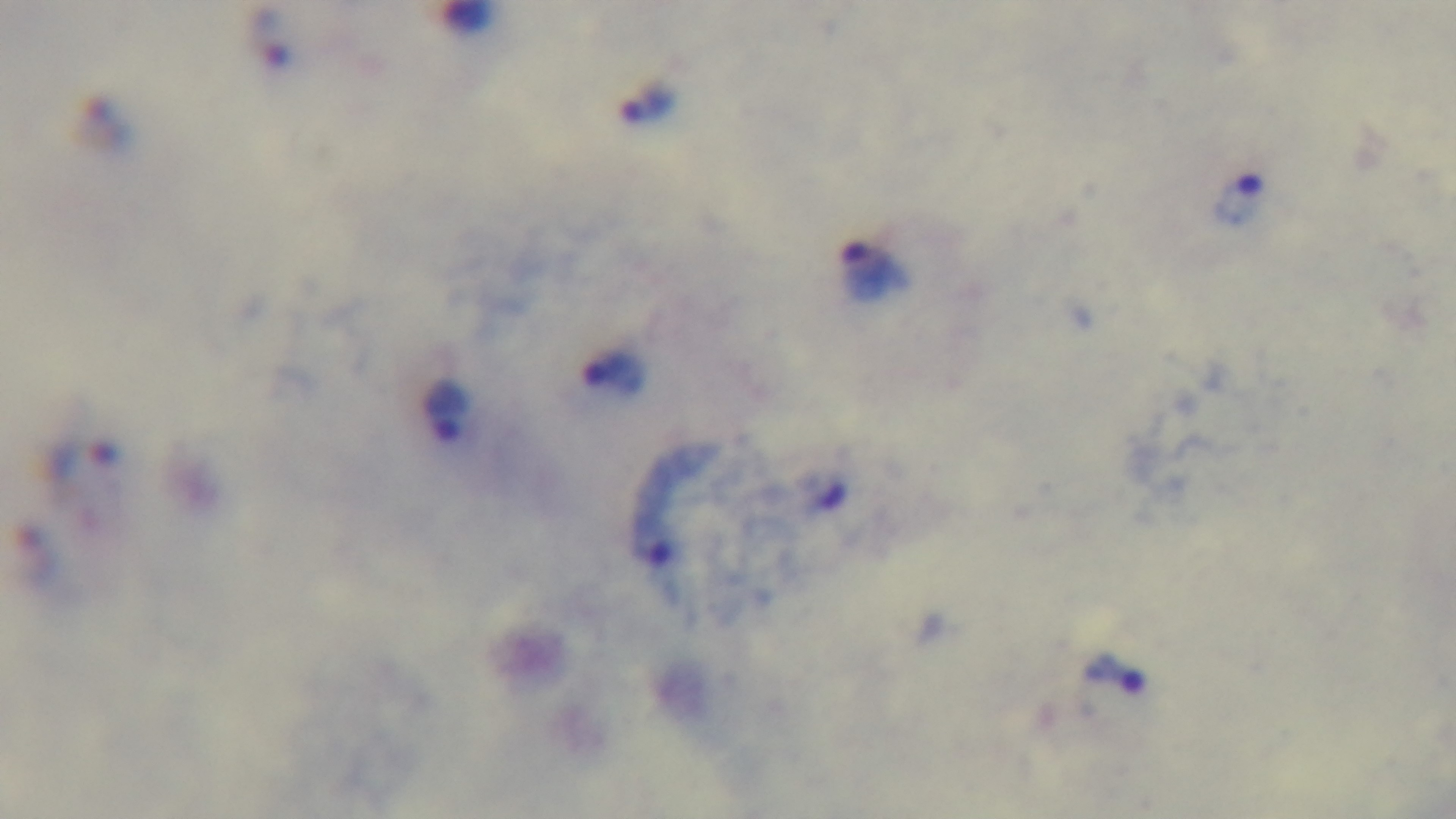

Summary:
  - Stain: Giemsa
  - Field of view: single
  - Modality: light microscopy
  - Objective: 100x oil immersion
  - Capture: mounted 4K digital camera
  - Malaria status: infected
  - Preparation: thick